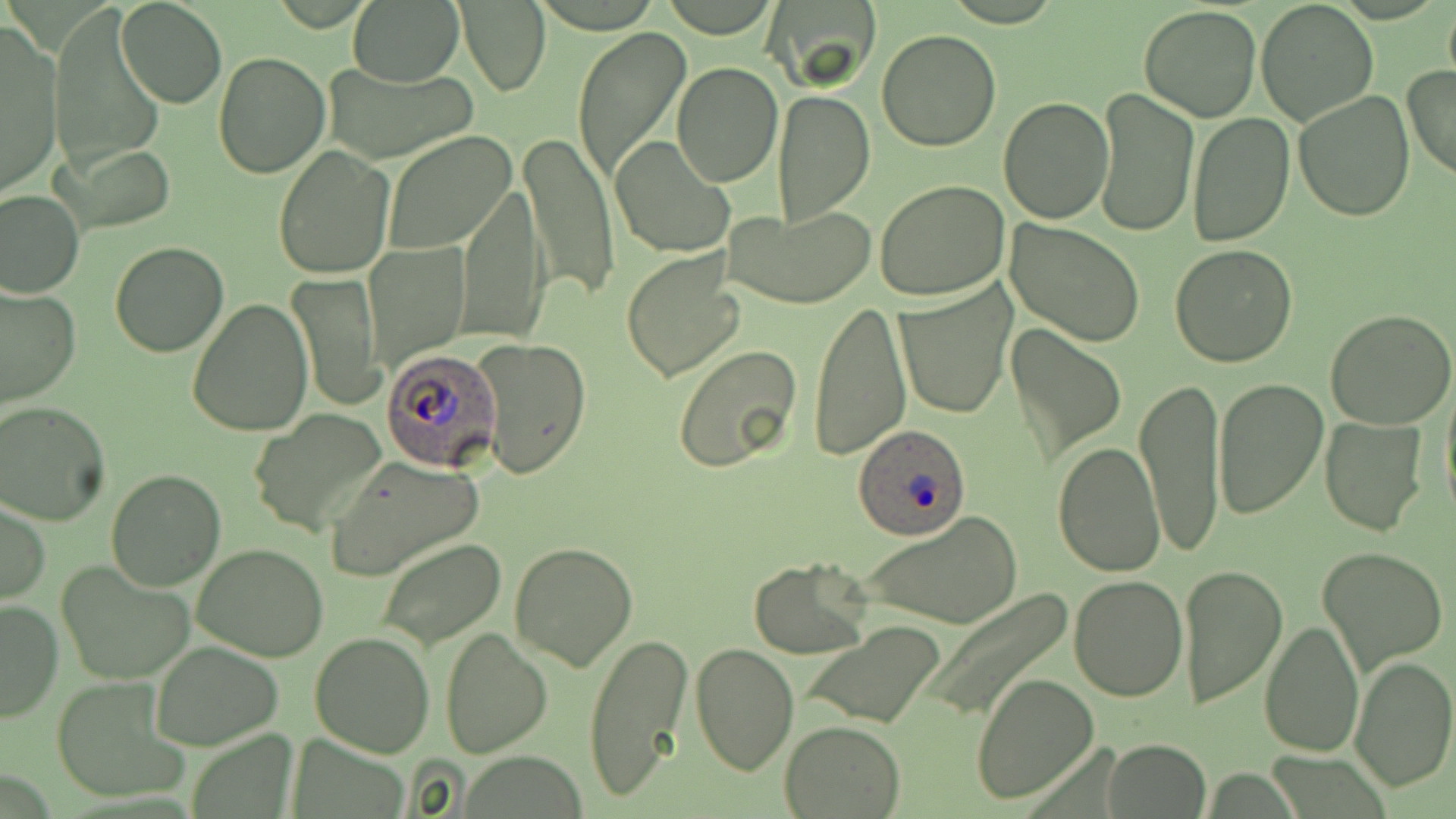
Summary:
  - Coordinate format: approximate bounding boxes as (x1,y1)-(x2,y2) corner pairs in pixels
  - Uninfected red blood cell locations: (348,0)-(465,88), (766,0)-(879,89), (1256,0)-(1380,126), (116,1)-(226,109), (1442,2)-(1456,91), (458,3)-(550,95), (1138,5)-(1262,123), (50,8)-(165,177), (2,26)-(62,197), (573,26)-(691,184), (877,29)-(1002,152), (213,54)-(330,178), (324,62)-(479,162), (670,62)-(782,187), (1403,66)-(1456,183), (1093,86)-(1198,237), (772,90)-(875,224), (1294,90)-(1415,223), (998,95)-(1114,224), (1187,110)-(1296,247), (383,130)-(518,254), (520,131)-(619,303), (609,135)-(737,258), (63,144)-(177,233), (274,145)-(395,281), (875,180)-(1011,302), (458,182)-(547,347), (0,187)-(84,298), (723,204)-(875,309), (1005,221)-(1144,346), (364,241)-(469,369), (109,242)-(229,357), (1168,245)-(1298,368), (620,249)-(746,381), (290,273)-(383,411), (894,284)-(1015,418), (1,285)-(78,409), (186,298)-(311,436), (810,300)-(911,461), (1326,307)-(1456,429), (1006,323)-(1126,463), (474,337)-(591,481), (672,346)-(805,474), (1440,375)-(1456,524), (1135,377)-(1227,556), (1210,377)-(1327,521), (0,401)-(109,525), (248,409)-(387,538), (1320,415)-(1428,536), (1051,440)-(1165,577), (323,456)-(484,581), (106,469)-(228,591), (1,499)-(49,605), (860,509)-(1024,630), (375,538)-(507,649), (508,539)-(638,672), (193,544)-(331,661), (1316,546)-(1448,675), (748,557)-(874,657), (55,561)-(194,685), (1177,565)-(1288,711), (1067,574)-(1187,701), (924,589)-(1075,720), (0,597)-(62,722), (1259,618)-(1365,757), (799,622)-(946,729), (440,625)-(553,758), (583,630)-(693,803), (310,631)-(435,756), (148,640)-(284,750), (690,642)-(798,777), (1349,655)-(1456,793), (971,672)-(1099,806), (50,678)-(189,805), (779,719)-(908,818), (1103,739)-(1210,818)
  - Plasmodium ovale-infected red blood cell locations: (378,348)-(498,471), (851,425)-(972,540)
  - Slide-level diagnosis: Plasmodium ovale
  - Image size: 1456×819 pixels
  - Preparation: thin blood film
  - Magnification: 1000x
  - Modality: optical microscopy
  - Stain: May-Grünwald-Giemsa
  - Field of view: single